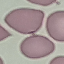

Result: no malaria parasites detected. Giemsa-stained preparation. Thin blood film. Acquired by smartphone through the microscope eyepiece. Automatically extracted cell patch, resized to 64 × 64 pixels.